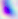

Summary:
  - Modality: photomicrograph
  - Identification: Toxoplasma gondii
  - Magnification: 400x